State which parasite is depicted.
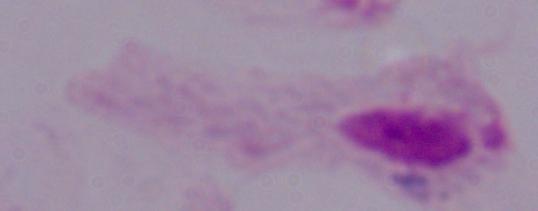
A trichomonad.

Summary:
  - Magnification: 1000x
  - Modality: micrograph